Assess this cell for malaria.
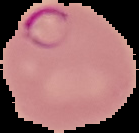

Parasitized.

Image is 139×133 pixels. From a thin blood smear. Cell region segmented out of the field of view; the surrounding area is masked to black.